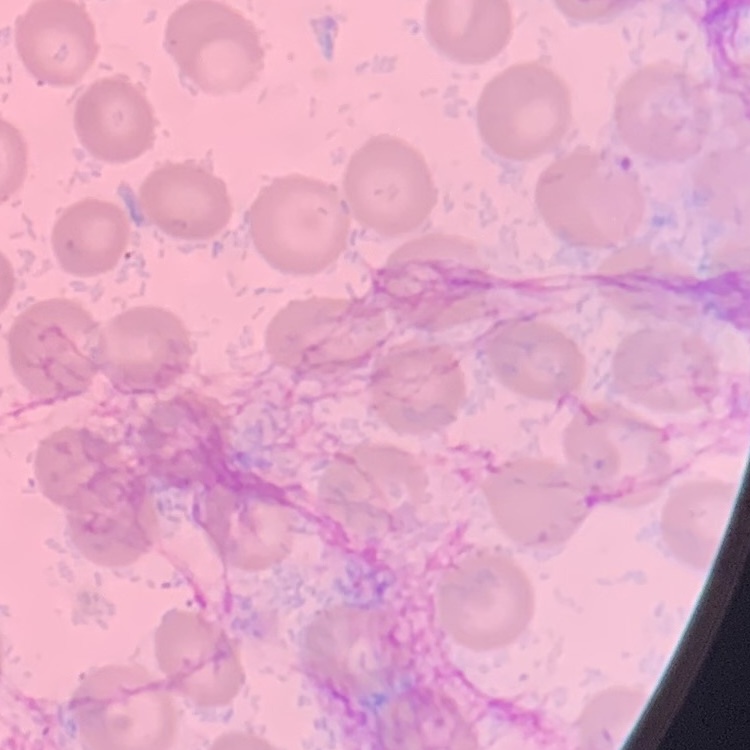
Summary:
  - Red blood cell morphology: no rouleaux formation
  - Preparation: thin blood film
  - Image type: one tile cut from a larger photomicrograph
  - Stain: Field's or Giemsa